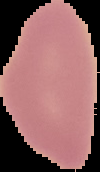

{
  "malaria_status": "uninfected",
  "image_size": "100×172 pixels",
  "preparation": "thin blood smear",
  "image_type": "segmented cell region on a black background"
}